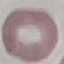
Malaria status: uninfected. Acquired by smartphone through the microscope eyepiece. Thin blood smear. Cell patch, automatically extracted from a larger field of view and resized to 64 × 64 pixels. Giemsa-stained preparation.